Name the parasite shown.
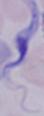
This is a trypanosome.

modality: micrograph
magnification: 1000x